Report the malaria status of this cell.
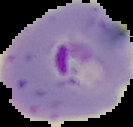
It is parasitized.

preparation = thin blood film
image size = 133×127 pixels
image type = segmented cell region on a black background